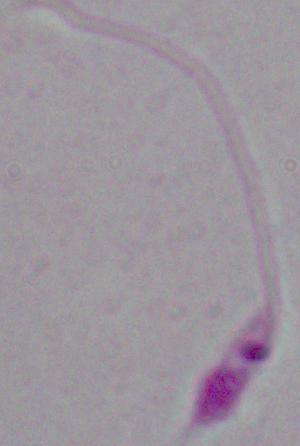

magnification = 1000x
modality = micrograph
identification = Leishmania